Locate leukocytes (white blood cells).
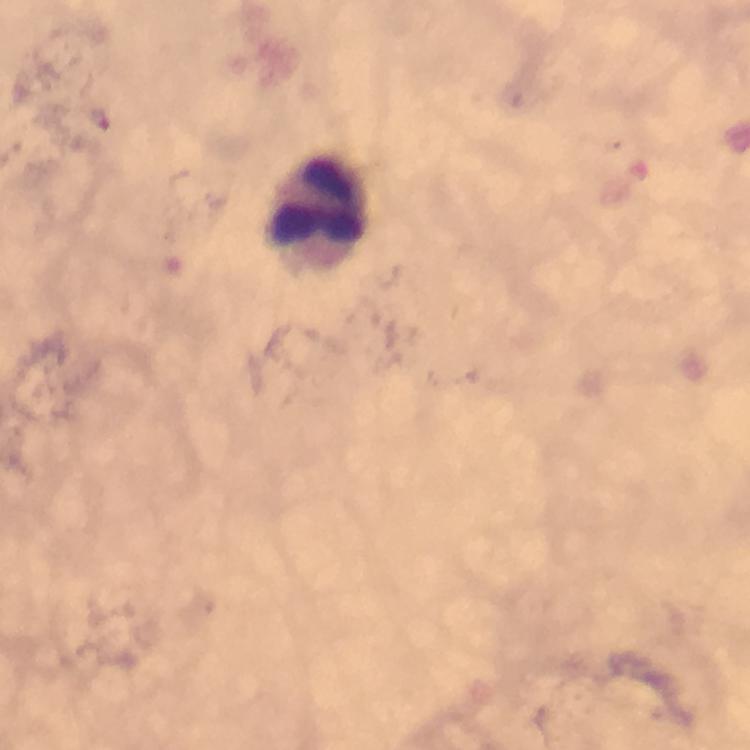

Approximate object centers, in pixels from the top-left corner.
Leukocytes: (x=318, y=209).

Plasmodium parasite locations: (x=97, y=120). 100x magnification. From a diagnostic examination for malaria. Thick blood smear. Giemsa stain. Smartphone photograph taken through a microscope. Immersion oil applied. Cropped region of a single field of view. Image is 750×750 pixels.